Evaluate for malaria.
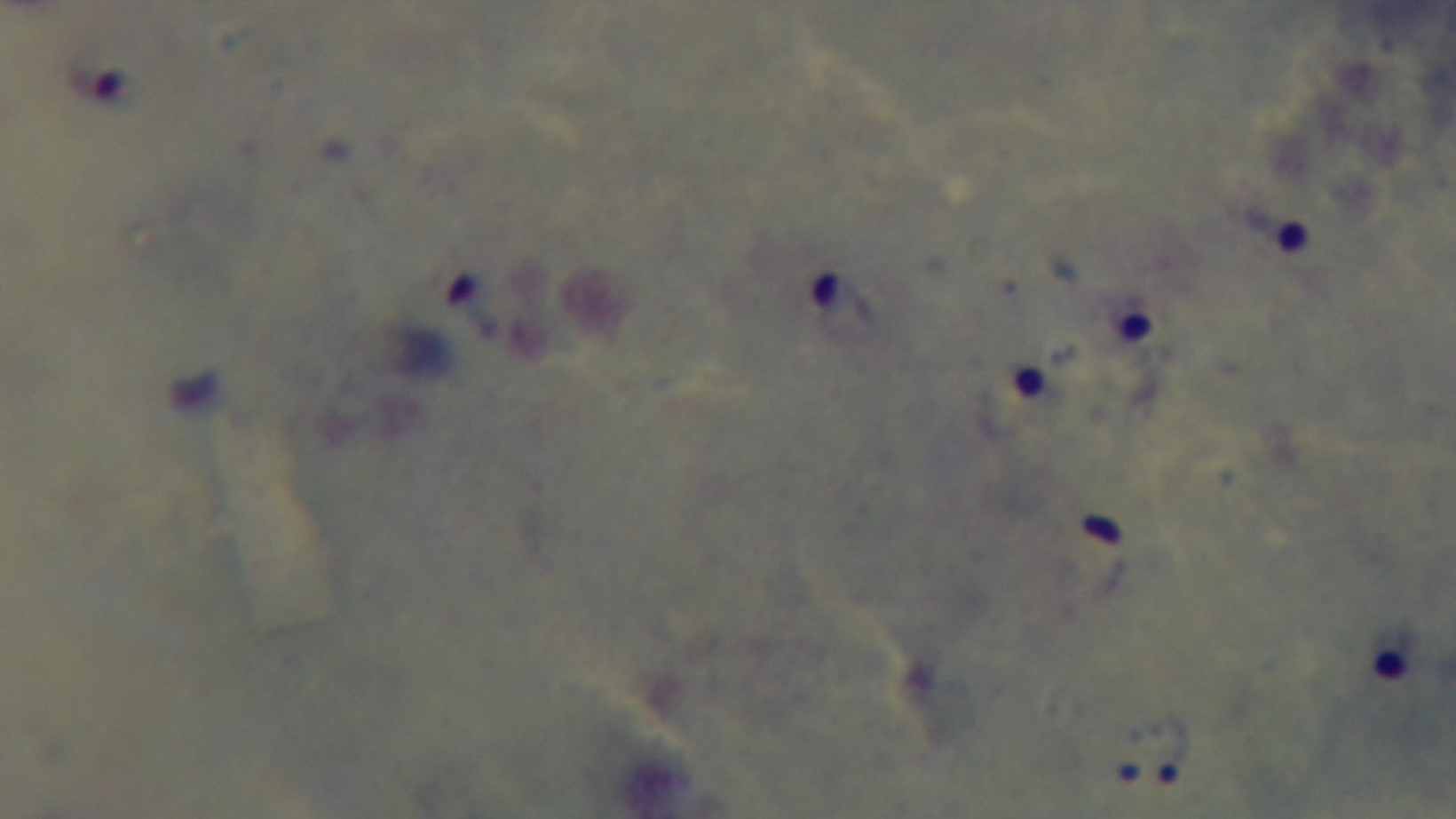
Infected.

Summary:
  - Preparation: thick
  - Capture: mounted 4K digital camera
  - Objective: 100x oil immersion
  - Modality: light microscopy
  - Field of view: single
  - Stain: Giemsa